Classify this cell by malaria status.
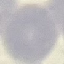

Uninfected.

Acquired by smartphone through the microscope eyepiece. Cell patch, automatically extracted from a larger field of view and resized to 64 × 64 pixels. Giemsa-stained preparation. Thin blood smear.